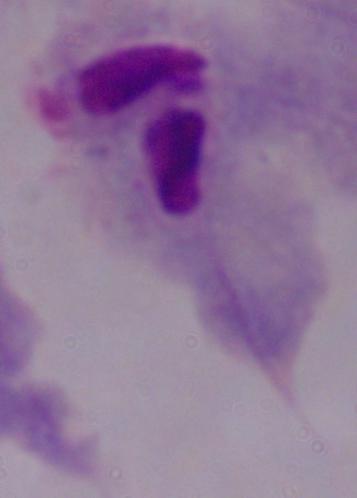

Summary:
  - Magnification: 1000x
  - Modality: micrograph
  - Identification: trichomonad